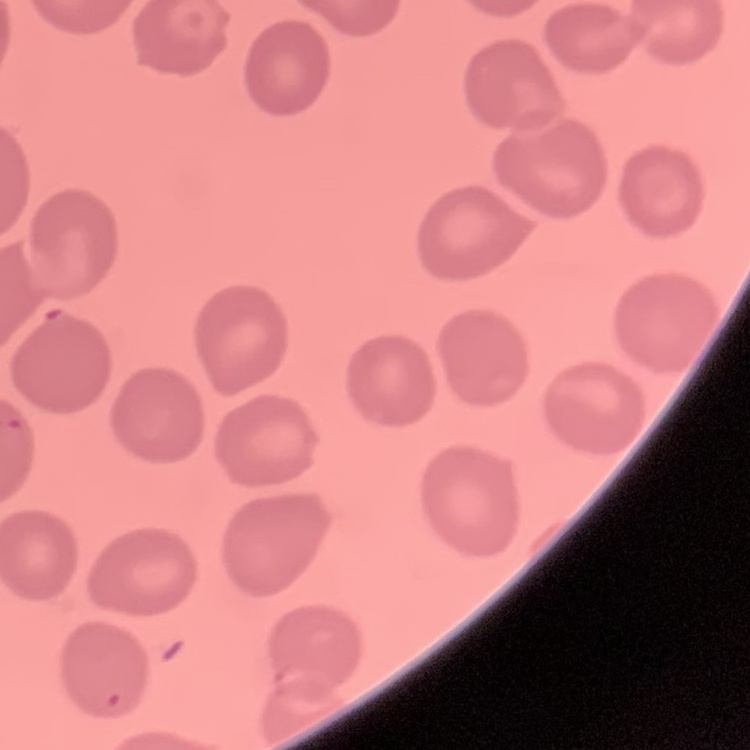
The erythrocytes show no rouleaux formation. Thin blood film. Square crop of a larger photomicrograph. Stained with either Field's or Giemsa.